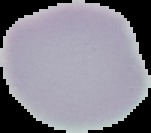 Malaria status: uninfected. From a thin blood smear. Segmented cell region on a black background. Image is 151×133 pixels.